Name the cell type shown.
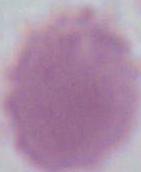

An erythrocyte.

magnification = 1000x
modality = photomicrograph